Assess this cell for malaria.
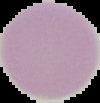
It is uninfected.

image type = segmented cell region with the area outside set to black
preparation = thin blood film
image size = 100×103 pixels